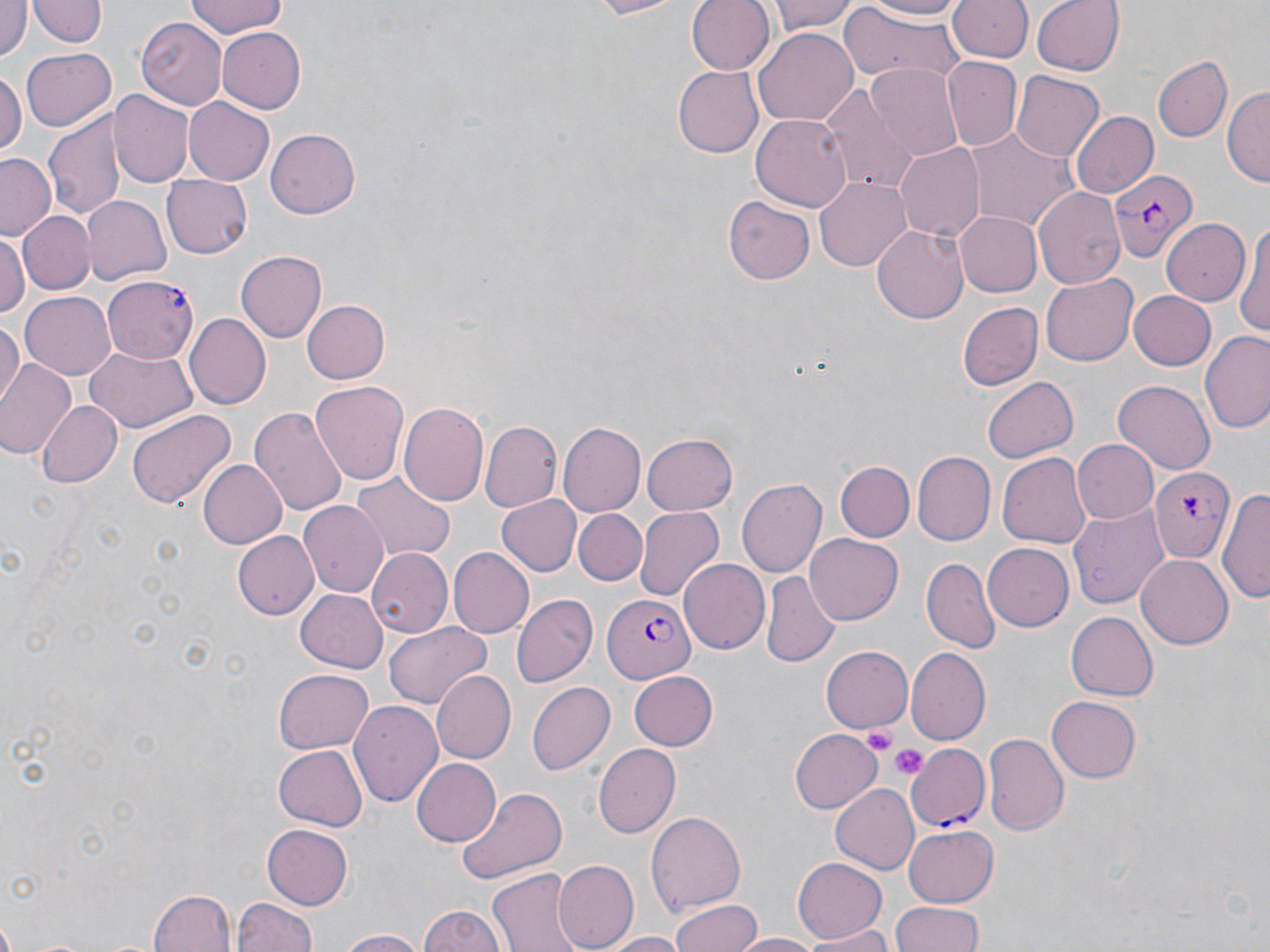
slide-level diagnosis = Plasmodium falciparum
image size = 1270×952 pixels
stain = May-Grünwald-Giemsa
uninfected red blood cell locations = approximate bounding boxes as (x1,y1)-(x2,y2) corner pairs in pixels: (183,0)-(291,38), (574,0)-(691,20), (686,0)-(775,76), (769,0)-(859,35), (859,0)-(971,22), (1030,0)-(1125,77), (30,1)-(103,49), (950,1)-(1032,63), (0,3)-(28,62), (838,5)-(966,82), (138,19)-(226,109), (216,26)-(307,113), (752,28)-(858,127), (21,47)-(116,132), (1155,57)-(1232,142), (941,58)-(1021,151), (674,64)-(764,155), (866,64)-(962,156), (0,66)-(25,153), (1010,71)-(1104,163), (821,85)-(916,191), (1225,86)-(1269,189), (109,91)-(194,189), (183,97)-(274,186), (46,107)-(127,225), (1070,110)-(1158,199), (751,114)-(852,209), (960,125)-(1077,230), (265,128)-(360,219), (895,140)-(985,240), (1,152)-(58,239), (159,174)-(252,260), (814,175)-(913,268), (1033,186)-(1125,289), (723,195)-(813,283), (81,196)-(172,284), (16,209)-(94,293), (956,212)-(1041,297), (1161,217)-(1249,305), (1234,218)-(1270,345), (873,222)-(970,322), (0,231)-(27,327), (234,251)-(327,344), (1041,272)-(1138,365), (20,290)-(117,378), (1126,291)-(1217,371), (955,292)-(1116,382), (300,298)-(390,386), (959,302)-(1043,391), (185,314)-(271,409), (0,318)-(22,408), (1200,330)-(1270,434), (85,345)-(196,432), (0,359)-(76,460), (983,376)-(1080,463), (310,381)-(407,484), (1114,381)-(1215,472), (37,401)-(120,487), (400,401)-(492,507), (248,407)-(346,516), (127,409)-(235,510), (480,421)-(560,514), (558,421)-(646,518), (642,431)-(739,515), (1072,440)-(1160,523), (915,451)-(997,546), (996,452)-(1092,547), (197,458)-(288,550), (836,462)-(914,542), (351,474)-(452,559), (737,477)-(828,578), (1222,485)-(1270,608), (496,495)-(582,577), (1068,500)-(1168,609), (299,502)-(388,597), (634,507)-(722,600), (573,509)-(647,584), (233,529)-(318,619), (803,535)-(904,625), (981,544)-(1072,632), (449,547)-(533,639), (367,549)-(452,639), (1135,554)-(1232,650), (922,558)-(999,653), (677,559)-(769,653), (761,573)-(839,666), (295,588)-(386,673), (513,596)-(595,686), (1064,610)-(1156,702), (383,620)-(492,710), (820,644)-(913,733), (904,649)-(988,745), (273,669)-(373,755), (433,670)-(516,762), (627,671)-(718,752), (527,682)-(615,776), (1046,695)-(1141,782), (353,701)-(443,809), (788,729)-(882,813), (983,735)-(1067,839), (594,743)-(680,838), (272,744)-(366,832), (411,759)-(500,846), (831,784)-(918,873), (454,786)-(568,884), (646,811)-(746,915), (262,825)-(352,909), (901,825)-(999,909), (791,858)-(886,943), (555,860)-(636,951), (488,868)-(583,952), (148,888)-(236,951), (232,896)-(318,952), (671,897)-(764,952), (891,903)-(988,952), (417,906)-(508,952), (798,927)-(898,951), (335,929)-(427,952), (597,933)-(692,952), (730,933)-(824,951)
modality = light microscopy
preparation = thin blood smear
Plasmodium falciparum-infected red blood cell locations = approximate bounding boxes as (x1,y1)-(x2,y2) corner pairs in pixels: (1107,169)-(1198,263), (104,273)-(200,361), (1152,464)-(1233,561), (604,591)-(696,683), (906,743)-(990,833)
field of view = single
platelet locations = approximate bounding boxes as (x1,y1)-(x2,y2) corner pairs in pixels: (859,722)-(897,752), (890,744)-(927,780)
magnification = 1000x